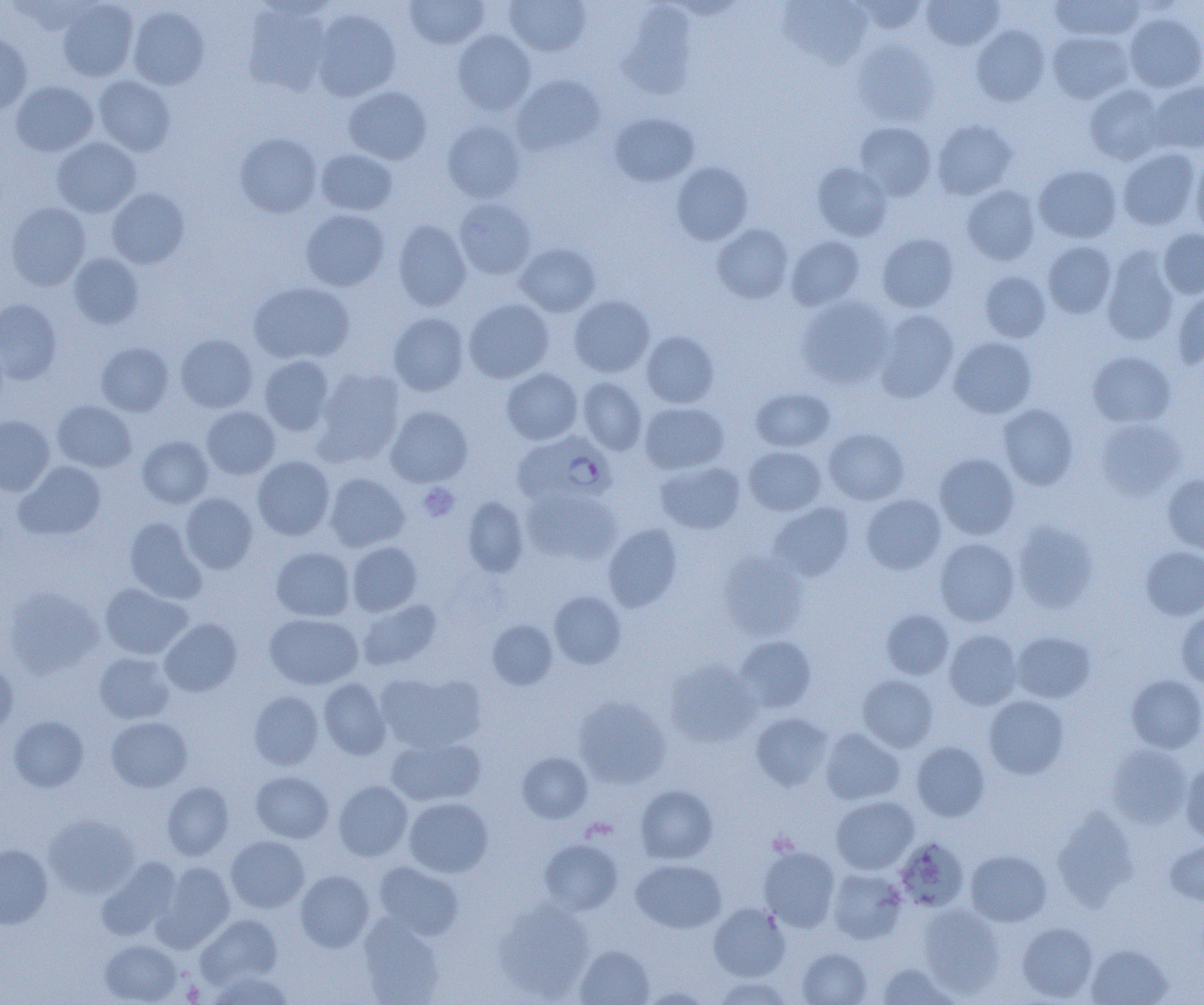

Approximate bounding boxes as (x1, y1, x2, y2) in pixels. Platelet locations: (418, 483, 460, 522), (183, 980, 204, 1003). Plasmodium falciparum-infected red blood cell locations: (514, 431, 617, 505). Uninfected red blood cell locations: (404, 0, 489, 49), (504, 0, 591, 56), (853, 0, 929, 34), (921, 0, 1004, 51), (1051, 0, 1145, 42), (56, 1, 139, 81), (779, 1, 873, 69), (243, 4, 331, 96), (127, 6, 210, 90), (312, 9, 401, 101), (1123, 11, 1204, 92), (971, 25, 1050, 106), (453, 29, 536, 115), (0, 31, 32, 115), (1047, 31, 1134, 104), (852, 39, 938, 126), (512, 74, 606, 155), (93, 75, 176, 156), (11, 80, 98, 157), (1146, 81, 1204, 153), (1084, 84, 1167, 165), (343, 86, 431, 164), (609, 112, 700, 187), (932, 119, 1017, 200), (442, 120, 526, 203), (854, 121, 937, 201), (235, 133, 321, 217), (52, 137, 140, 217), (1117, 147, 1201, 230), (315, 149, 397, 216), (1191, 152, 1204, 239), (671, 162, 753, 245), (812, 162, 892, 240), (1034, 164, 1122, 244), (962, 185, 1041, 265), (107, 188, 189, 269), (453, 198, 537, 279), (6, 202, 91, 291), (300, 209, 390, 291), (392, 219, 471, 311), (712, 224, 794, 304), (1158, 229, 1204, 299), (877, 233, 959, 312), (785, 235, 865, 310), (1042, 241, 1117, 319), (515, 243, 601, 317), (1101, 247, 1180, 346), (68, 253, 144, 328), (979, 271, 1051, 343), (248, 282, 353, 364), (1172, 287, 1204, 369), (568, 295, 655, 377), (796, 295, 895, 390), (463, 298, 554, 383), (0, 299, 61, 384), (874, 309, 959, 402), (388, 312, 469, 396), (641, 331, 720, 408), (175, 334, 257, 413), (949, 336, 1037, 418), (95, 342, 174, 416), (1087, 350, 1176, 428), (258, 355, 335, 436), (313, 368, 405, 467), (501, 368, 583, 445), (577, 377, 647, 455), (750, 387, 835, 451), (52, 400, 137, 472), (640, 402, 729, 474), (998, 404, 1079, 490), (201, 406, 280, 479), (385, 406, 473, 487), (0, 416, 55, 495), (1095, 418, 1186, 500), (823, 428, 909, 505), (137, 436, 213, 508), (744, 445, 827, 516), (934, 453, 1020, 540), (252, 456, 335, 540), (15, 461, 107, 539), (655, 461, 746, 535), (324, 472, 409, 552), (1162, 473, 1204, 555), (520, 486, 620, 566), (180, 492, 258, 573), (861, 494, 946, 574), (461, 496, 529, 577), (768, 502, 855, 581), (124, 517, 206, 602), (1013, 521, 1098, 613), (603, 523, 682, 612), (935, 538, 1020, 626), (347, 541, 422, 616), (271, 546, 355, 621), (1141, 546, 1204, 620), (718, 550, 809, 640), (100, 583, 192, 659), (4, 587, 104, 678), (549, 590, 626, 669), (357, 599, 442, 671), (1174, 609, 1204, 687), (881, 610, 954, 679), (264, 613, 363, 689), (160, 618, 242, 696), (487, 619, 558, 690), (944, 629, 1023, 709), (1012, 631, 1095, 703), (733, 635, 817, 714), (94, 652, 175, 724), (664, 658, 762, 747), (0, 659, 17, 734), (376, 671, 487, 753), (857, 674, 939, 751), (1126, 674, 1204, 752), (318, 677, 391, 759), (249, 691, 323, 770), (983, 695, 1069, 779), (573, 696, 671, 788), (750, 712, 832, 791), (8, 715, 89, 791), (106, 717, 192, 792), (820, 728, 904, 805), (386, 736, 485, 806), (911, 741, 990, 822), (1107, 743, 1192, 828), (517, 752, 593, 823), (1180, 761, 1204, 845), (250, 770, 333, 843), (333, 781, 413, 861), (162, 782, 233, 860), (635, 784, 719, 864), (831, 796, 919, 874), (403, 797, 493, 877), (1053, 806, 1138, 911), (44, 814, 139, 897), (226, 835, 309, 912), (894, 836, 969, 912), (539, 839, 622, 914), (1166, 840, 1204, 905), (0, 844, 53, 928), (758, 845, 840, 931), (965, 849, 1052, 926), (96, 858, 180, 941), (631, 859, 727, 933), (374, 860, 463, 940), (155, 862, 235, 950), (826, 868, 906, 944), (295, 870, 373, 952), (493, 900, 594, 1001), (709, 903, 790, 981), (918, 904, 1005, 998), (358, 914, 446, 1004), (197, 915, 282, 987), (1016, 922, 1098, 1002), (99, 939, 184, 1004), (1086, 944, 1173, 1005), (574, 945, 655, 1005), (797, 948, 872, 1005), (876, 962, 959, 1004), (208, 971, 294, 1004), (712, 976, 794, 1004), (641, 986, 713, 1004). Slide-level diagnosis: Plasmodium falciparum. Captured at 1000x magnification. Single field of view. Image is 1204×1005 pixels. Optical microscopy. Thin blood film.